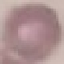
Summary:
  - Result: no malaria parasites seen
  - Capture: smartphone camera at the microscope eyepiece
  - Image type: cell patch, automatically extracted from a larger field of view and resized to 64 × 64 pixels
  - Stain: Giemsa
  - Preparation: thin blood smear